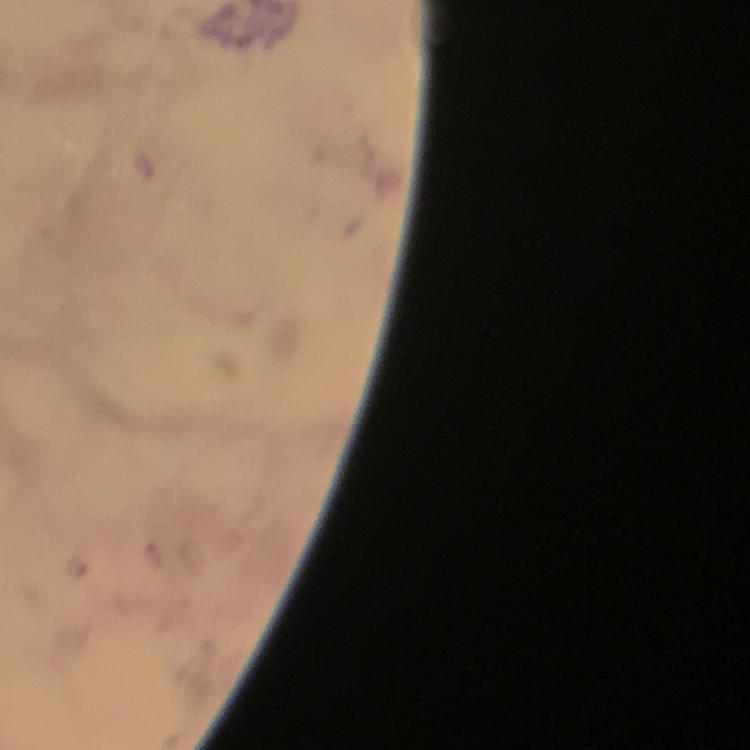
{
  "magnification": "100x",
  "preparation": "thick smear",
  "capture": "smartphone camera through the microscope",
  "immersion_oil": "applied",
  "cropped_from": "one field of view",
  "malaria_parasite_locations": "approximate object centers, in pixels from the top-left corner: (x=154, y=553), (x=74, y=563)",
  "stain": "Giemsa",
  "image_size": "750×750 pixels",
  "context": "from a malaria diagnostic workup"
}